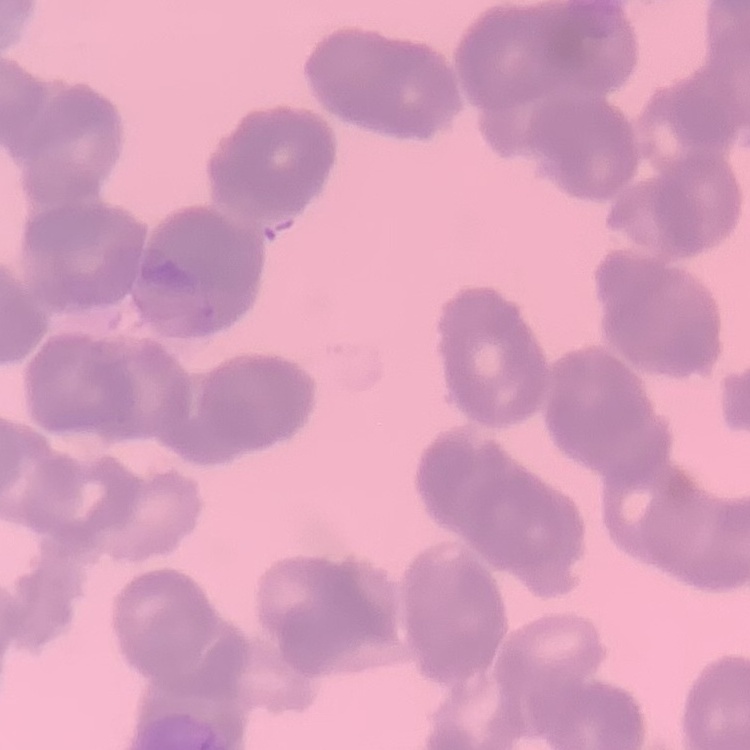

The erythrocytes show rouleaux formation. Stained with either Field's or Giemsa. Square crop of a larger photomicrograph. Thin blood film.